Identify the parasite.
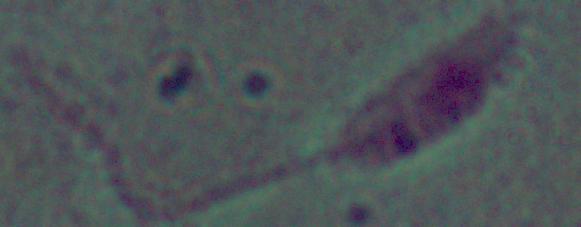
Leishmania.

Photomicrograph. 1000x magnification.